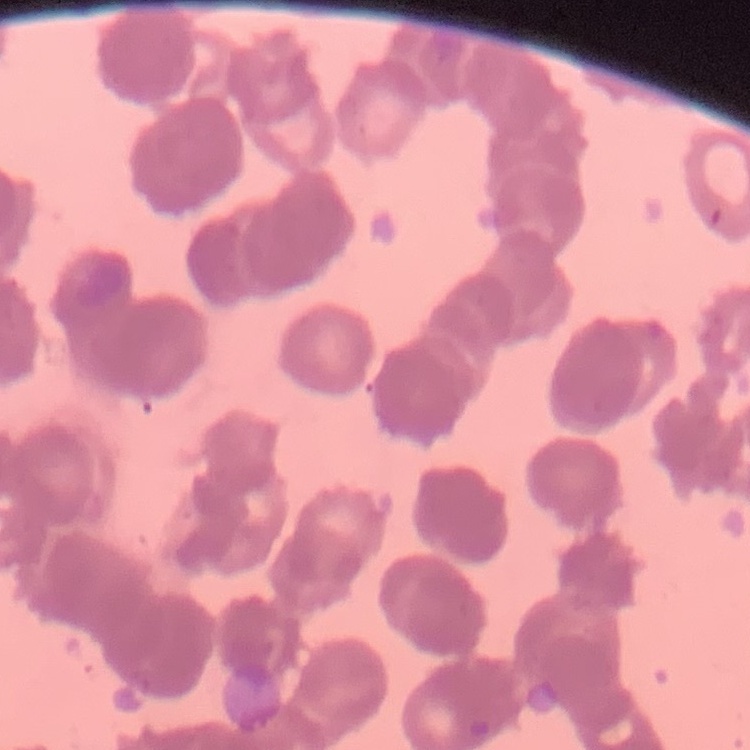 The erythrocytes show rouleaux formation. Square crop of a larger photomicrograph. Thin blood smear. Field's or Giemsa stain.